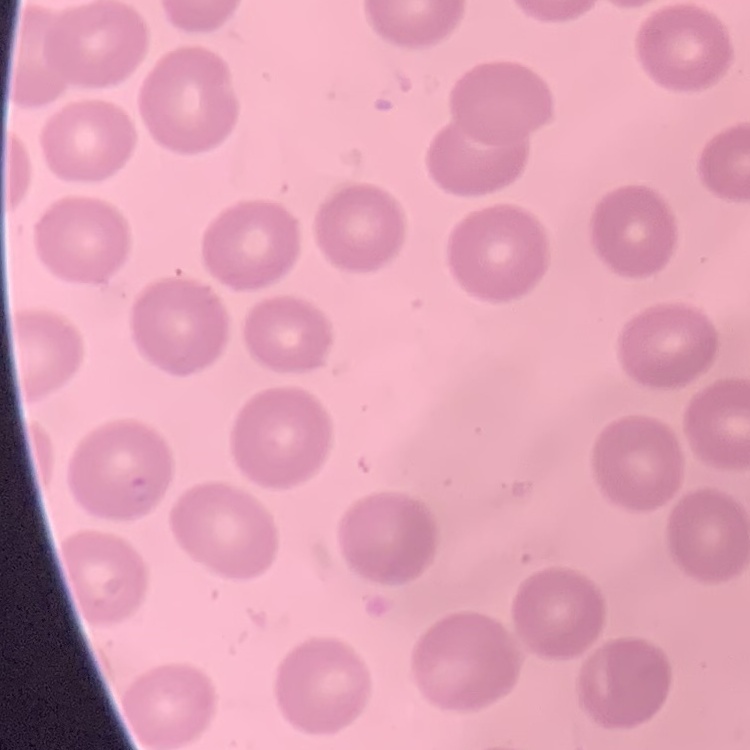

Summary:
  - Red blood cell morphology: no rouleaux formation
  - Image type: square crop of a larger photomicrograph
  - Preparation: thin blood smear
  - Stain: Field's or Giemsa